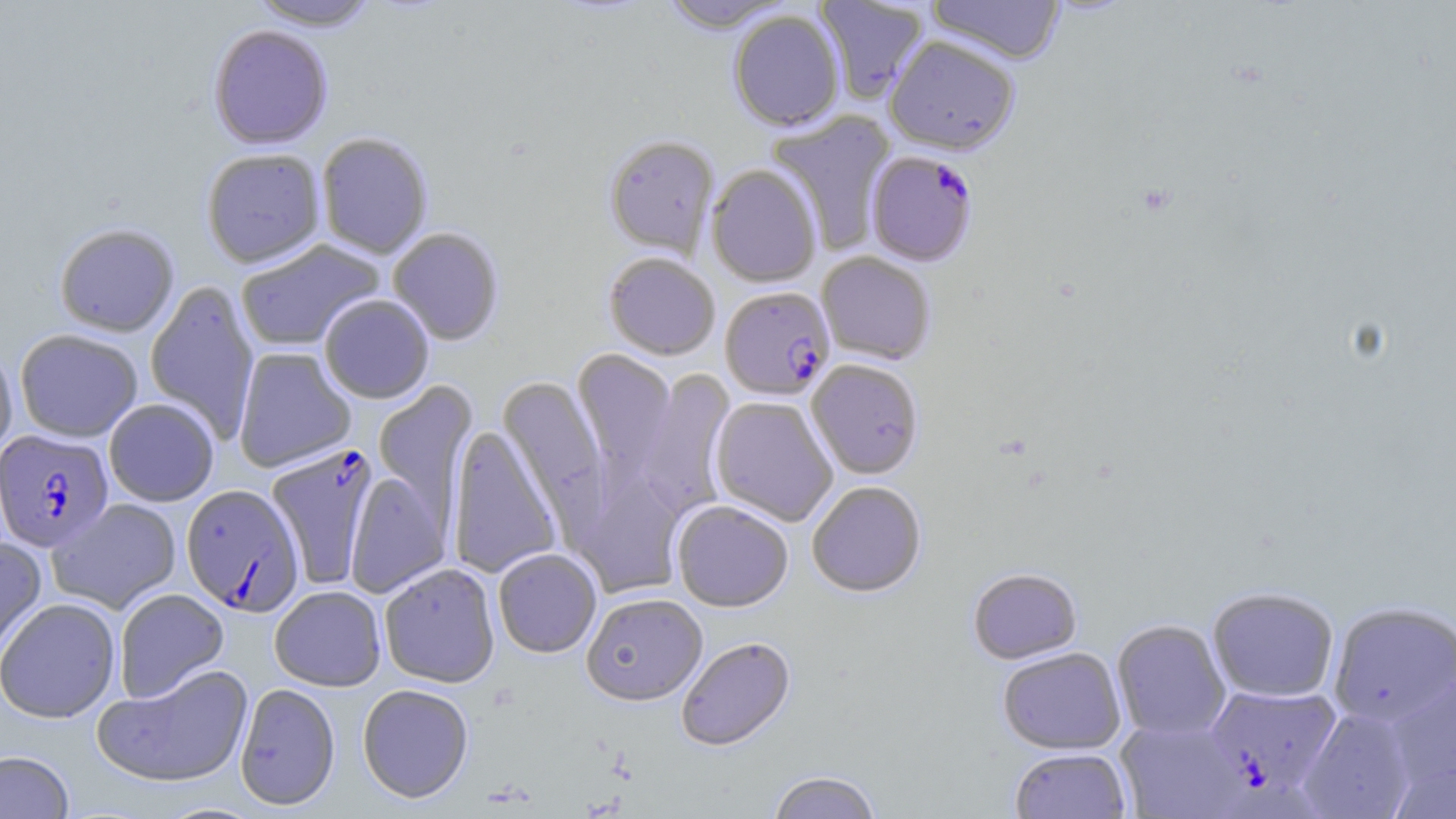 Approximate bounding boxes as (x1,y1)-(x2,y2) corner pairs in pixels. Uninfected red blood cell locations: (248,0)-(381,31), (815,0)-(929,104), (927,0)-(1066,65), (659,1)-(795,34), (728,10)-(845,131), (208,26)-(333,151), (884,36)-(1020,155), (767,110)-(897,254), (316,133)-(433,260), (603,135)-(720,258), (201,150)-(326,270), (706,164)-(822,287), (53,224)-(180,338), (388,228)-(505,346), (235,239)-(387,352), (603,252)-(720,360), (816,252)-(936,365), (144,280)-(260,443), (319,295)-(434,404), (15,329)-(143,443), (0,342)-(18,465), (233,347)-(356,472), (572,349)-(678,482), (806,359)-(923,479), (632,368)-(736,520), (497,376)-(609,524), (372,380)-(479,531), (710,396)-(837,526), (104,399)-(219,507), (447,424)-(562,580), (574,462)-(687,599), (345,471)-(450,598), (807,481)-(927,597), (47,498)-(182,614), (672,500)-(793,612), (0,536)-(48,665), (493,548)-(602,659), (379,563)-(500,689), (967,567)-(1082,664), (269,586)-(386,691), (1207,587)-(1339,702), (114,588)-(229,703), (582,594)-(708,707), (1,598)-(121,724), (1328,602)-(1456,727), (1111,619)-(1230,740), (676,637)-(796,752), (997,647)-(1126,754), (91,663)-(254,791), (1384,671)-(1456,789), (234,684)-(341,812), (357,684)-(474,804), (1298,706)-(1420,818), (1115,717)-(1247,819), (1010,747)-(1131,818), (0,751)-(74,819), (1390,758)-(1456,819), (766,771)-(883,819). Plasmodium falciparum-infected red blood cell locations: (866,150)-(978,267), (720,286)-(835,401), (0,429)-(114,552), (266,444)-(380,589), (180,484)-(305,618), (1203,683)-(1342,800). Slide-level diagnosis: Plasmodium falciparum. Optical microscopy. Image is 1456×819 pixels. Thin blood film. One field of a larger specimen. Captured at 1000x magnification. May-Grünwald-Giemsa stain.